Point out each Plasmodium parasite.
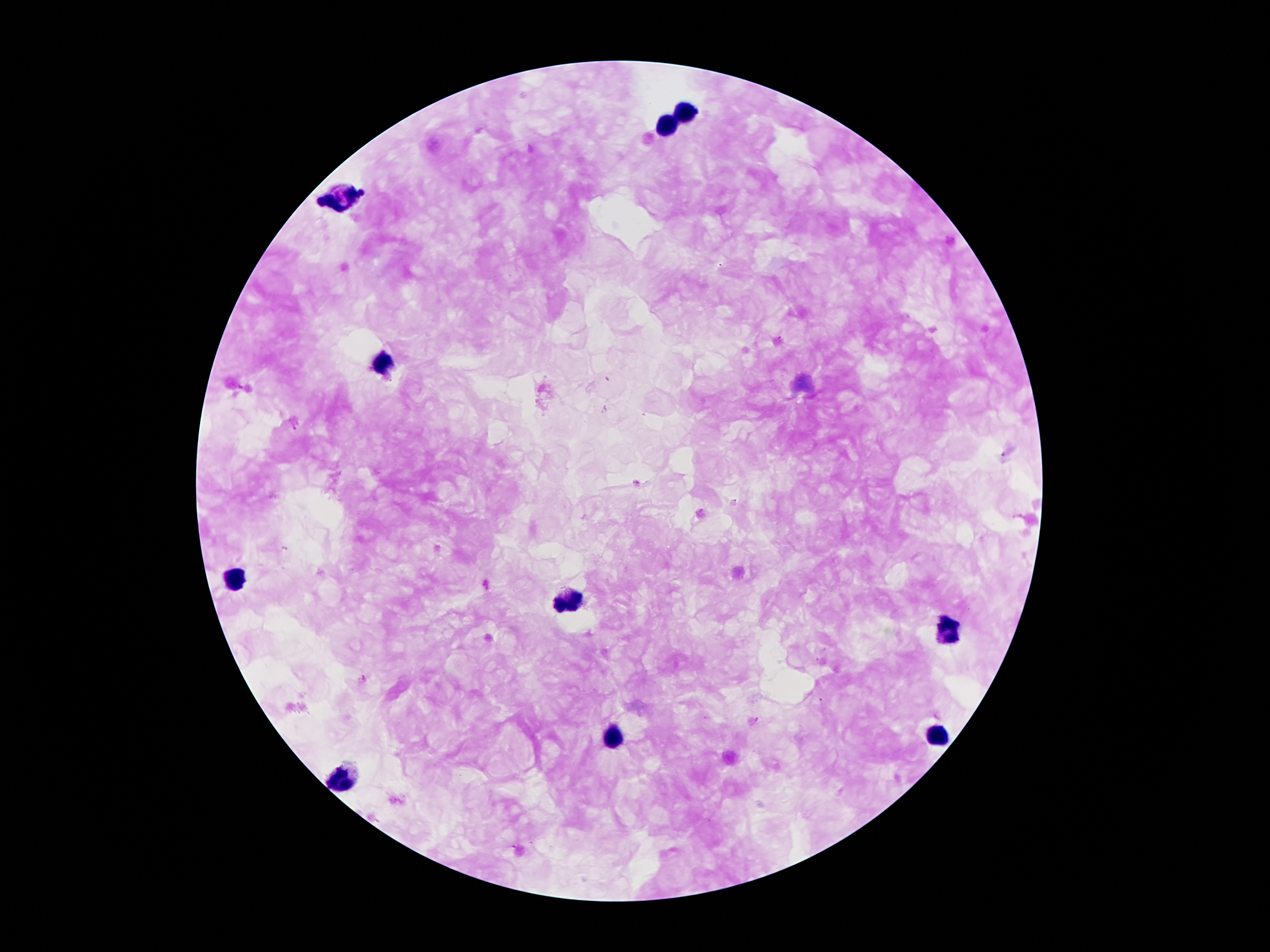

No Plasmodium parasites identified.

Approximate centers as [x, y] in pixels.
Summary:
  - Leukocyte locations: [683, 108], [666, 124], [341, 194], [383, 363], [234, 578], [571, 601], [947, 630], [941, 734], [609, 736], [344, 780]
  - Capture: smartphone camera through the microscope eyepiece
  - Magnification: 100x
  - Preparation: thick blood smear
  - Field of view: single
  - Patient malaria status: infected with Plasmodium falciparum
  - Image size: 1270×952 pixels
  - Stain: Giemsa